Comment on the morphology of the red blood cells.
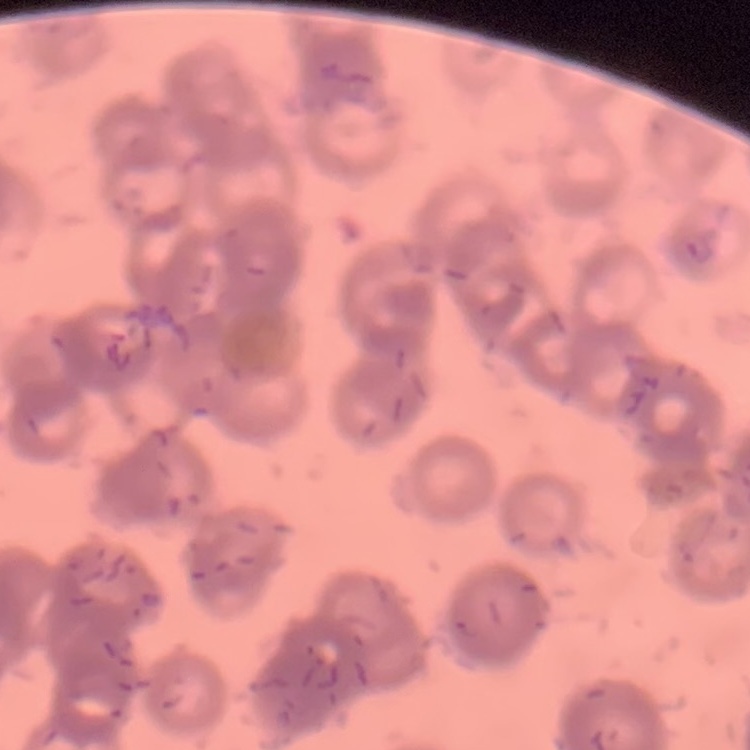

Rouleaux formation.

Summary:
  - Preparation: thin blood smear
  - Image type: square crop of a larger photomicrograph
  - Stain: Field's or Giemsa